Describe the morphology of the erythrocytes.
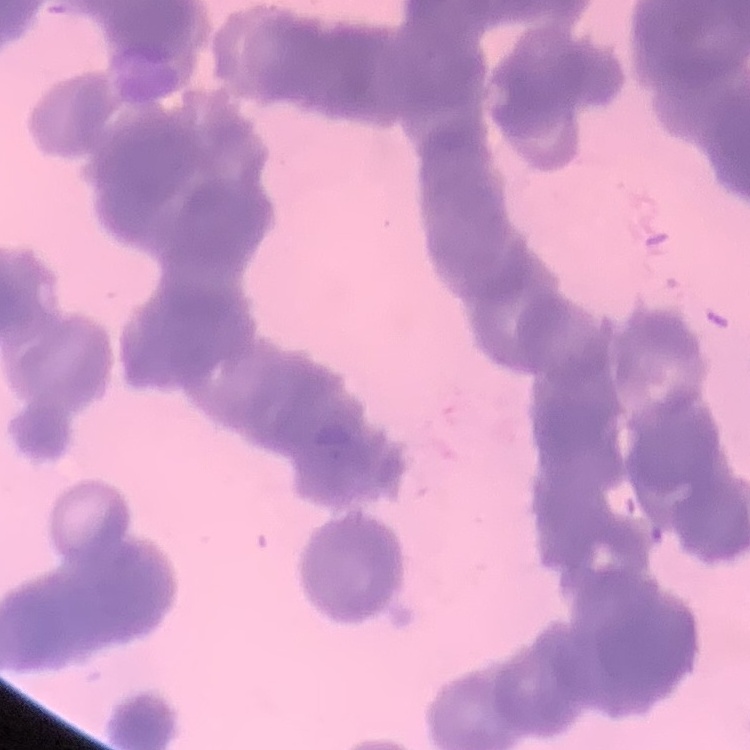
Rouleaux formation.

Summary:
  - Preparation: thin blood film
  - Image type: one tile cut from a larger photomicrograph
  - Stain: Field's or Giemsa